Locate every malaria parasite.
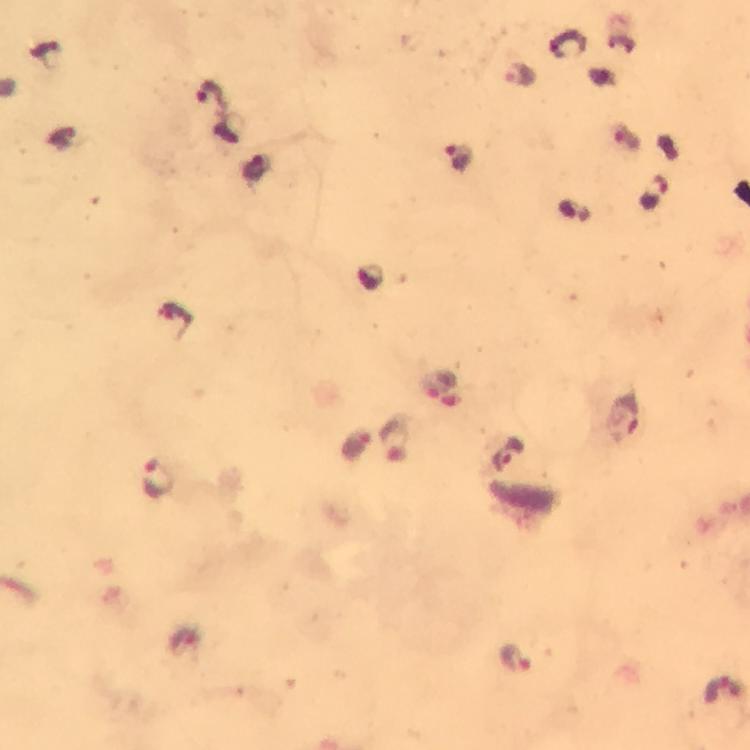

Approximate centers as (x, y) in pixels.
Malaria parasites: (519, 75), (459, 160), (654, 197), (438, 385), (625, 417), (507, 456), (158, 478), (515, 658), (723, 692).

Summary:
  - Stain: Giemsa
  - Capture: smartphone mounted on the microscope
  - Image size: 750×750 pixels
  - Cropped from: a single field of view
  - Immersion oil: applied
  - Context: from a malaria diagnostic workup
  - Preparation: thick blood smear
  - Magnification: 100x